Locate and identify every blood parasite.
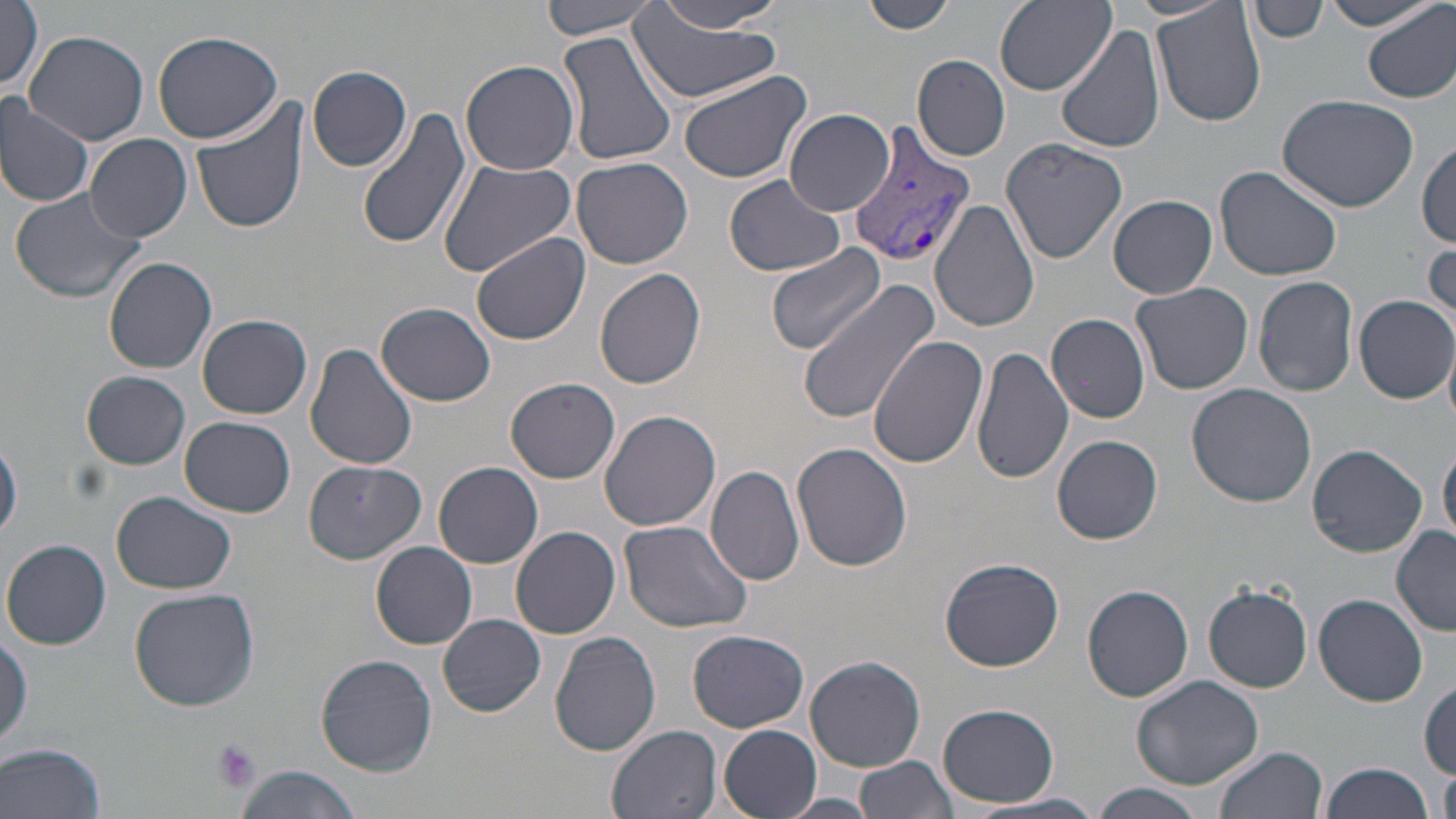
Approximate bounding boxes as named x1/y1/x2/y2 corners in pixels.
Plasmodium vivax-infected red blood cells: (x1=847, y1=122, x2=976, y2=270).
No Plasmodium falciparum, Plasmodium ovale, Plasmodium malariae, Babesia divergens, or Trypanosoma brucei observed.

slide-level diagnosis = Plasmodium vivax
preparation = thin blood film
modality = light microscopy
stain = May-Grünwald-Giemsa
field of view = single
uninfected red blood cell locations = approximate bounding boxes as named x1/y1/x2/y2 corners in pixels: (x1=1, y1=0, x2=43, y2=96), (x1=541, y1=0, x2=661, y2=40), (x1=860, y1=0, x2=954, y2=34), (x1=991, y1=0, x2=1115, y2=97), (x1=1251, y1=1, x2=1327, y2=44), (x1=1151, y1=2, x2=1268, y2=131), (x1=1321, y1=2, x2=1438, y2=30), (x1=1364, y1=3, x2=1456, y2=104), (x1=648, y1=4, x2=788, y2=36), (x1=626, y1=8, x2=784, y2=105), (x1=1054, y1=23, x2=1164, y2=154), (x1=23, y1=29, x2=148, y2=146), (x1=557, y1=29, x2=678, y2=169), (x1=152, y1=30, x2=284, y2=144), (x1=912, y1=54, x2=1011, y2=162), (x1=461, y1=58, x2=580, y2=176), (x1=307, y1=65, x2=411, y2=172), (x1=675, y1=67, x2=811, y2=185), (x1=1277, y1=94, x2=1420, y2=211), (x1=0, y1=95, x2=97, y2=209), (x1=189, y1=96, x2=310, y2=236), (x1=356, y1=104, x2=470, y2=250), (x1=784, y1=110, x2=897, y2=215), (x1=85, y1=133, x2=193, y2=243), (x1=998, y1=137, x2=1129, y2=264), (x1=1416, y1=142, x2=1456, y2=248), (x1=436, y1=156, x2=579, y2=278), (x1=47, y1=157, x2=174, y2=284), (x1=571, y1=157, x2=694, y2=271), (x1=1212, y1=165, x2=1343, y2=282), (x1=724, y1=175, x2=846, y2=278), (x1=10, y1=188, x2=149, y2=307), (x1=1110, y1=195, x2=1217, y2=299), (x1=932, y1=199, x2=1042, y2=333), (x1=471, y1=232, x2=591, y2=346), (x1=1425, y1=243, x2=1456, y2=335), (x1=765, y1=244, x2=889, y2=358), (x1=105, y1=255, x2=217, y2=373), (x1=594, y1=268, x2=707, y2=389), (x1=1253, y1=275, x2=1358, y2=397), (x1=798, y1=282, x2=942, y2=421), (x1=1131, y1=283, x2=1254, y2=397), (x1=1355, y1=294, x2=1455, y2=403), (x1=1041, y1=301, x2=1246, y2=408), (x1=378, y1=302, x2=496, y2=406), (x1=1046, y1=312, x2=1151, y2=423), (x1=197, y1=313, x2=312, y2=419), (x1=869, y1=335, x2=989, y2=470), (x1=1443, y1=341, x2=1456, y2=432), (x1=306, y1=342, x2=418, y2=473), (x1=970, y1=347, x2=1075, y2=485), (x1=83, y1=371, x2=191, y2=469), (x1=506, y1=377, x2=621, y2=484), (x1=1186, y1=384, x2=1316, y2=507), (x1=598, y1=409, x2=723, y2=533), (x1=181, y1=416, x2=294, y2=517), (x1=1053, y1=435, x2=1163, y2=544), (x1=0, y1=438, x2=22, y2=543), (x1=1438, y1=440, x2=1456, y2=545), (x1=791, y1=442, x2=912, y2=574), (x1=1307, y1=443, x2=1428, y2=557), (x1=302, y1=459, x2=427, y2=563), (x1=433, y1=462, x2=544, y2=568), (x1=706, y1=465, x2=806, y2=586), (x1=112, y1=491, x2=236, y2=595), (x1=619, y1=521, x2=751, y2=636), (x1=510, y1=526, x2=622, y2=639), (x1=1391, y1=527, x2=1456, y2=636), (x1=3, y1=538, x2=110, y2=649), (x1=371, y1=541, x2=478, y2=648), (x1=939, y1=556, x2=1064, y2=672), (x1=1082, y1=581, x2=1195, y2=703), (x1=1203, y1=582, x2=1313, y2=693), (x1=127, y1=588, x2=259, y2=712), (x1=1315, y1=594, x2=1428, y2=708), (x1=438, y1=614, x2=546, y2=717), (x1=0, y1=629, x2=32, y2=751), (x1=688, y1=629, x2=808, y2=732), (x1=549, y1=631, x2=663, y2=755), (x1=316, y1=653, x2=439, y2=775), (x1=806, y1=655, x2=925, y2=770), (x1=1130, y1=674, x2=1264, y2=790), (x1=1418, y1=679, x2=1455, y2=777), (x1=938, y1=702, x2=1060, y2=807), (x1=605, y1=725, x2=725, y2=819), (x1=718, y1=725, x2=821, y2=819), (x1=2, y1=743, x2=108, y2=819), (x1=1214, y1=745, x2=1328, y2=819), (x1=856, y1=756, x2=957, y2=819), (x1=1318, y1=761, x2=1435, y2=819), (x1=233, y1=766, x2=366, y2=819), (x1=1439, y1=768, x2=1456, y2=819), (x1=1093, y1=783, x2=1209, y2=819), (x1=979, y1=793, x2=1102, y2=817), (x1=778, y1=795, x2=882, y2=818)
magnification = 1000x
platelet locations = approximate bounding boxes as named x1/y1/x2/y2 corners in pixels: (x1=210, y1=738, x2=264, y2=796)
image size = 1456×819 pixels